Assess this cell for malaria.
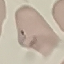
It is parasitized.

stain = Giemsa
preparation = thin blood smear
image type = automatically extracted cell patch, resized to 64 × 64 pixels
capture = smartphone camera at the microscope eyepiece